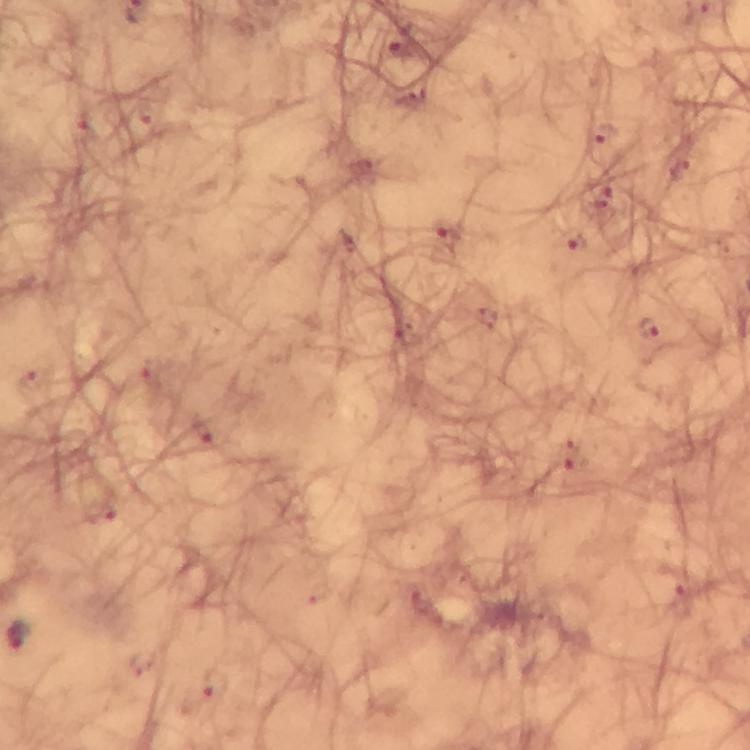

Approximate centers as {x, y} in pixels.
Summary:
  - Malaria parasite locations: {648, 329}
  - Immersion oil: used
  - Cropped from: one field of view
  - Context: from a diagnostic examination for malaria
  - Image size: 750×750 pixels
  - Capture: smartphone camera through the microscope
  - Magnification: 100x
  - Preparation: thick blood film
  - Stain: Giemsa